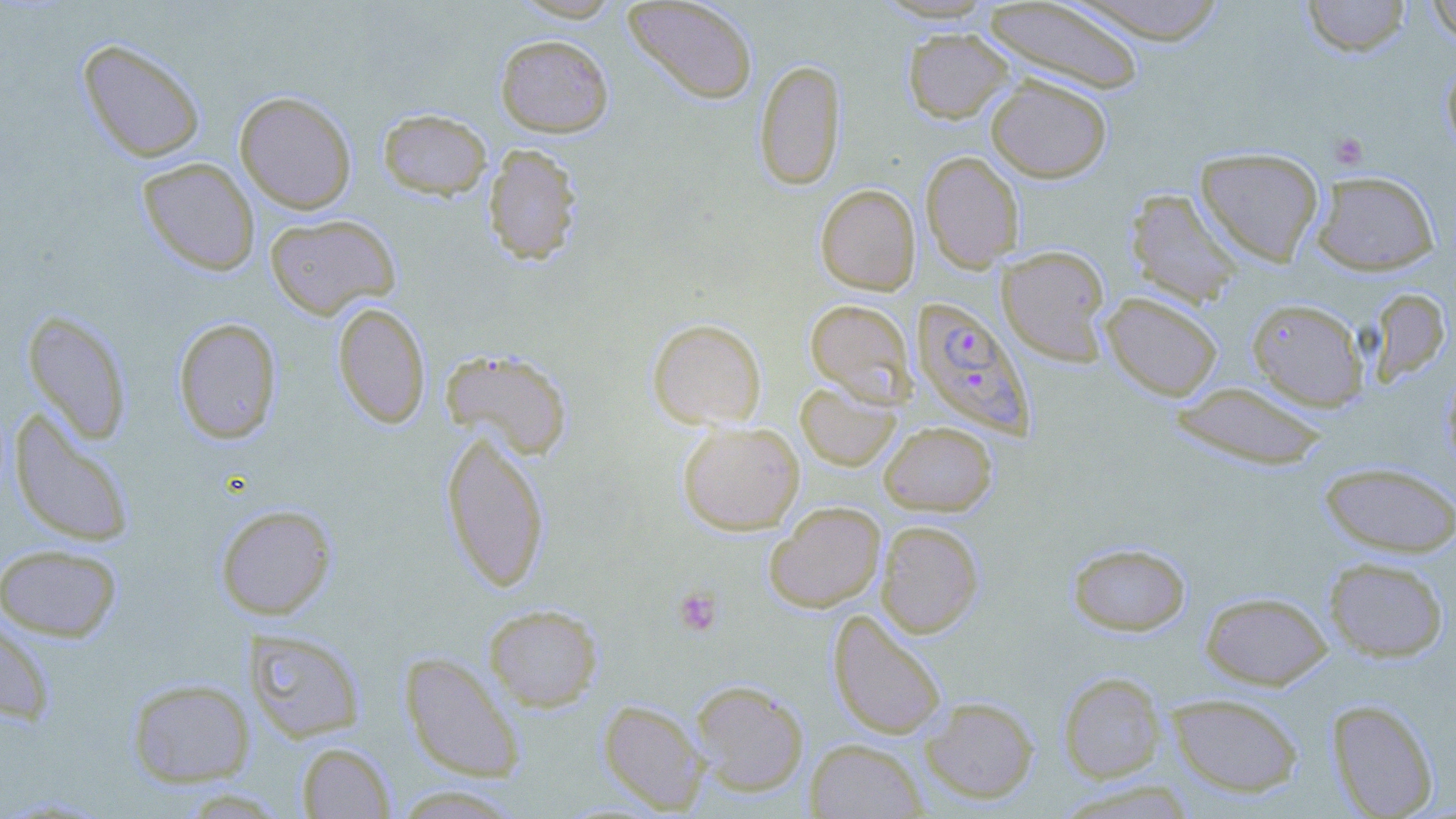
{
  "slide_level_diagnosis": "Plasmodium falciparum",
  "preparation": "thin blood film",
  "modality": "optical microscopy",
  "image_size": "1456×819 pixels",
  "uninfected_red_blood_cell_locations": "approximate bounding boxes as (x1,y1)-(x2,y2) corner pairs in pixels: (623,0)-(758,104), (984,0)-(1146,96), (1065,0)-(1229,44), (1301,0)-(1411,57), (1426,0)-(1456,44), (903,28)-(1013,123), (495,34)-(614,137), (77,38)-(206,163), (754,58)-(846,190), (1441,60)-(1456,159), (986,75)-(1112,182), (235,91)-(357,214), (378,108)-(492,199), (482,143)-(583,267), (1194,146)-(1325,266), (920,151)-(1025,271), (138,158)-(260,276), (1311,170)-(1440,275), (816,184)-(920,295), (1125,188)-(1245,309), (264,213)-(400,319), (997,245)-(1112,366), (1368,288)-(1451,384), (1101,292)-(1223,400), (805,298)-(916,405), (1247,298)-(1369,411), (332,302)-(431,429), (23,310)-(132,444), (173,317)-(282,444), (647,318)-(766,430), (439,348)-(573,460), (795,380)-(900,471), (1170,380)-(1329,471), (9,410)-(135,548), (879,421)-(997,516), (677,422)-(804,534), (440,428)-(551,593), (1319,462)-(1456,557), (765,502)-(885,612), (215,504)-(336,619), (876,520)-(984,638), (1068,542)-(1191,636), (0,543)-(123,642), (1324,556)-(1449,662), (1200,590)-(1332,689), (484,603)-(603,712), (828,611)-(947,740), (0,614)-(55,725), (243,628)-(366,742), (399,651)-(526,782), (1058,672)-(1167,783), (127,678)-(255,787), (691,680)-(809,797), (1166,694)-(1304,798), (920,695)-(1039,804), (598,699)-(709,814), (1327,699)-(1439,818), (805,738)-(927,818), (297,742)-(396,818), (390,785)-(526,818)",
  "field_of_view": "single",
  "plasmodium_falciparum_infected_red_blood_cell_locations": "approximate bounding boxes as (x1,y1)-(x2,y2) corner pairs in pixels: (911,296)-(1035,438)",
  "platelet_locations": "approximate bounding boxes as (x1,y1)-(x2,y2) corner pairs in pixels: (1329,131)-(1369,170), (673,586)-(722,635)",
  "stain": "May-Grünwald-Giemsa",
  "magnification": "1000x"
}